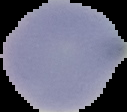

Summary:
  - Image type: segmented cell region on a black background
  - Malaria status: uninfected
  - Image size: 127×112 pixels
  - Preparation: thin blood smear